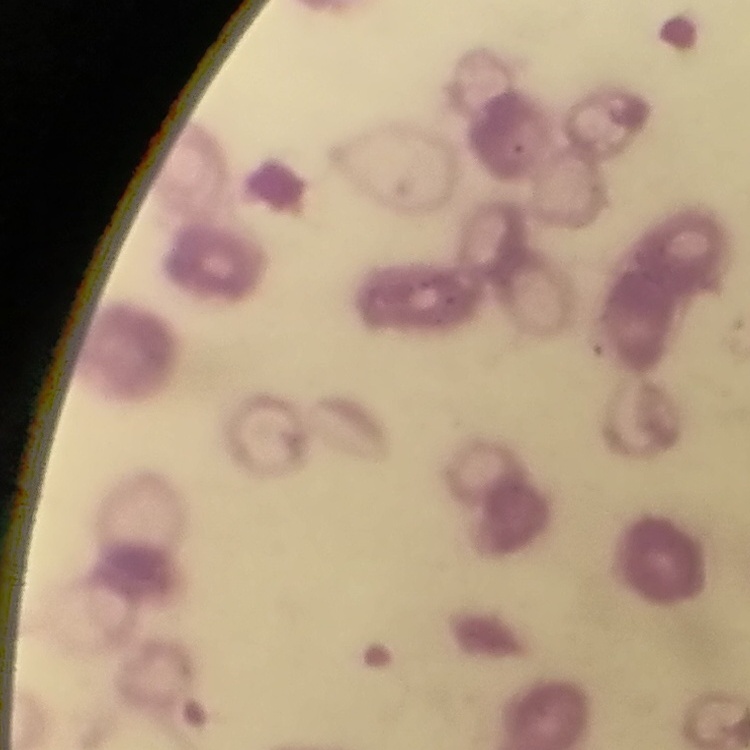
erythrocyte morphology = rouleaux formation
image type = one tile cut from a larger photomicrograph
stain = Field's or Giemsa
preparation = thin peripheral smear